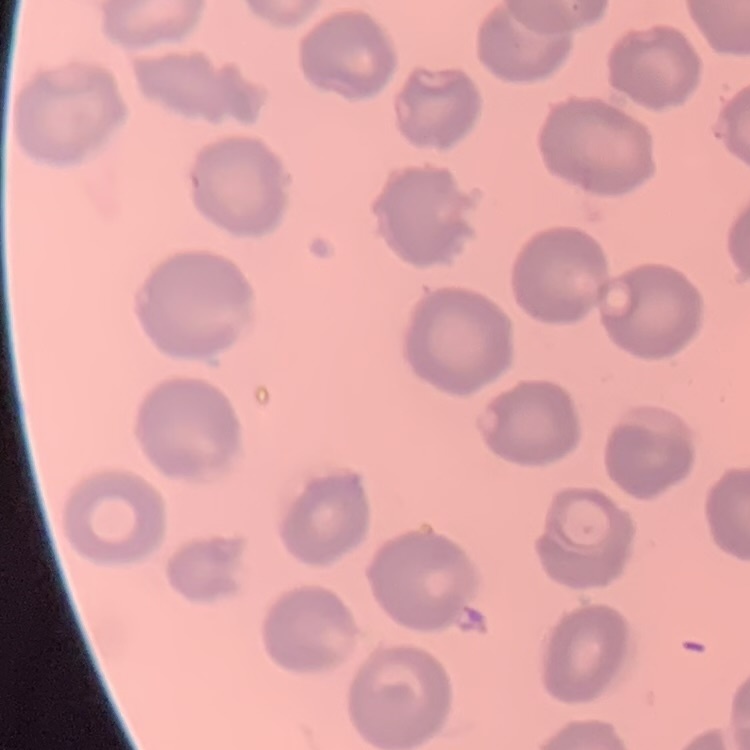
erythrocyte_morphology: no rouleaux formation
stain: Field's or Giemsa
image_type: square crop of a larger photomicrograph
preparation: thin blood smear